Identify the preparation type.
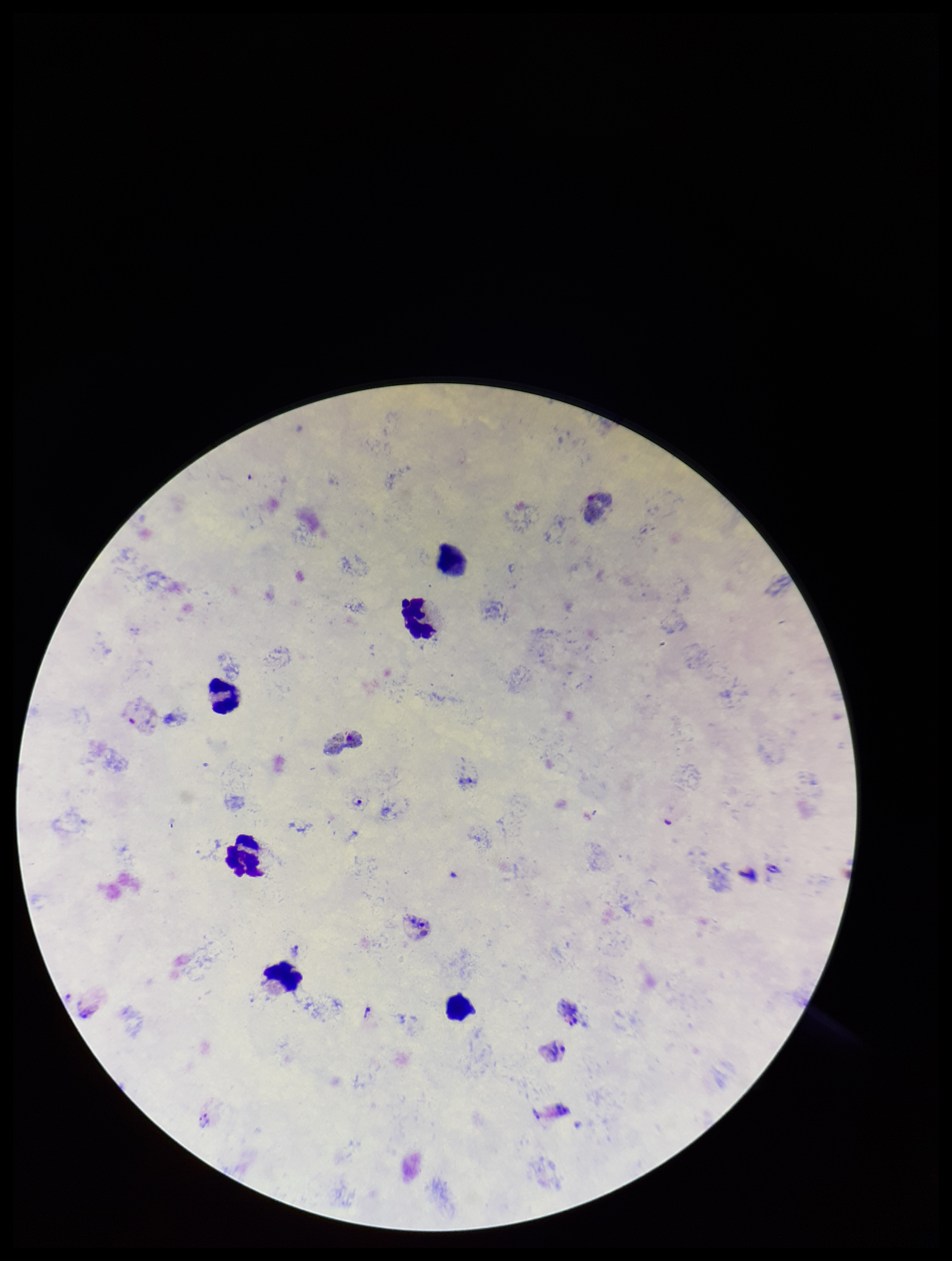
Thick.

Summary:
  - Leukocyte count: 6
  - Plasmodium parasites: identified
  - Species reported for this patient: Plasmodium vivax
  - Image size: 952×1261 pixels
  - Parasite count: 1
  - Field of view: single
  - Patient malaria status: positive
  - Stain: Giemsa
  - Capture: smartphone photograph through the microscope eyepiece